Report the malaria status of this cell.
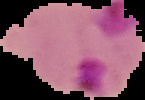
It is parasitized.

image size = 145×100 pixels
image type = segmented cell region on a black background
preparation = thin blood smear